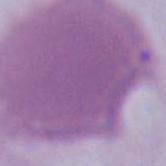

{
  "identification": "erythrocyte",
  "modality": "micrograph",
  "magnification": "1000x"
}